Report the malaria status of this cell.
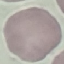
Uninfected.

Acquired by smartphone through the microscope eyepiece. Giemsa stain. Cell patch, automatically extracted from a larger field of view and resized to 64 × 64 pixels. Thin blood film.